Give a bounding box for every Plasmodium parasite, every leukocyte, and every artifact (stain precipitate or debris).
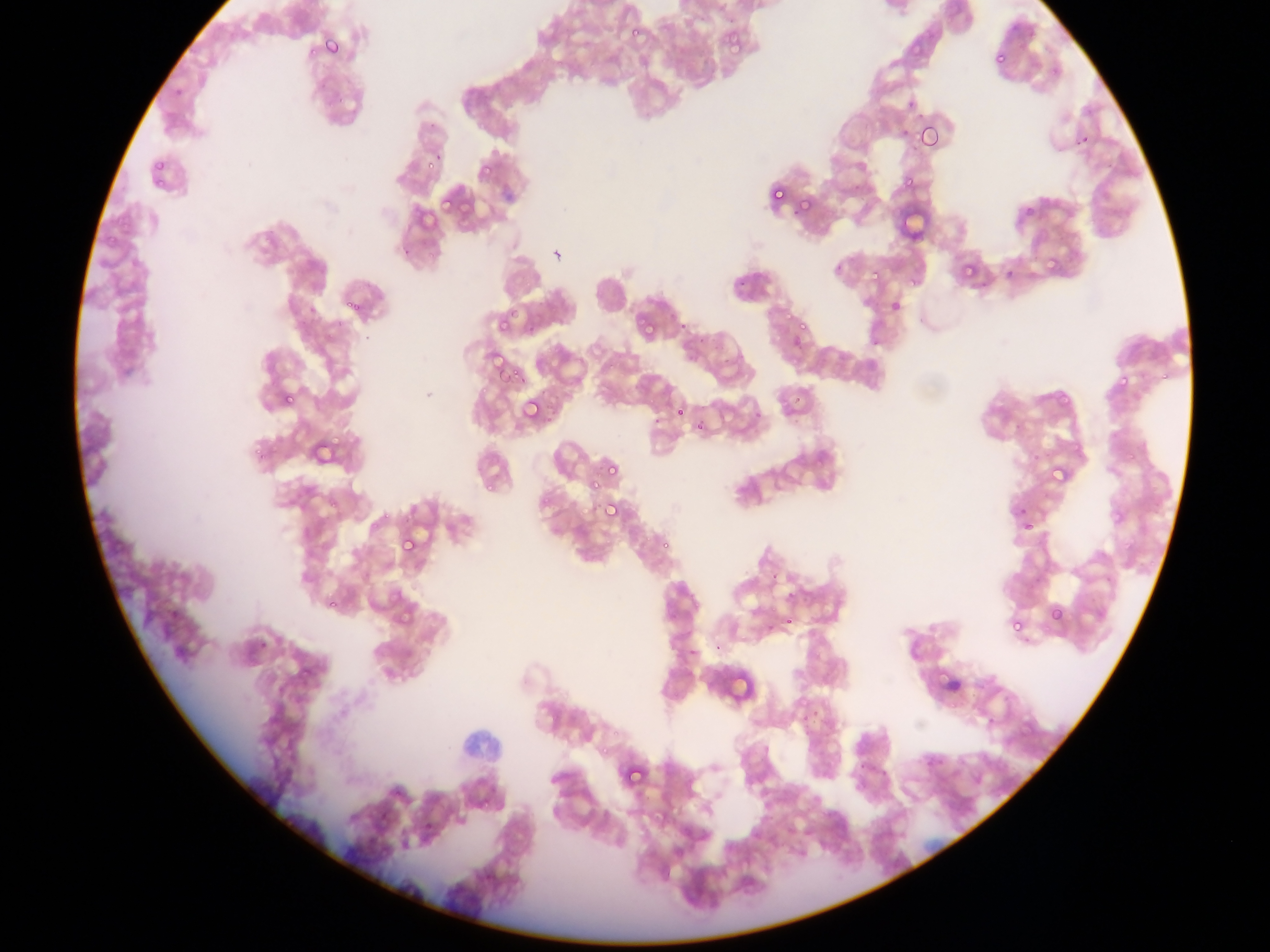

Approximate bounding boxes as [left, top, right, bottom] in pixels.
Plasmodium parasites: [626, 24, 648, 47], [719, 28, 744, 53], [312, 29, 347, 65], [904, 42, 925, 59], [990, 45, 1011, 67], [993, 51, 1007, 65], [917, 122, 943, 152], [150, 154, 172, 173], [899, 168, 917, 189], [770, 186, 786, 205], [803, 192, 816, 219], [435, 197, 461, 214], [1025, 207, 1036, 219], [411, 213, 442, 236], [958, 253, 983, 291], [1042, 256, 1059, 273], [870, 270, 887, 287], [344, 290, 375, 325], [887, 297, 905, 317], [781, 314, 793, 322], [640, 315, 664, 340], [497, 316, 518, 333], [797, 320, 814, 331], [789, 334, 806, 352], [497, 362, 526, 388], [1113, 370, 1145, 386], [1052, 382, 1077, 410], [278, 391, 295, 410], [520, 396, 544, 424], [674, 406, 688, 421], [694, 420, 709, 436], [604, 456, 617, 472], [1048, 461, 1073, 486], [601, 498, 623, 522], [1014, 503, 1033, 525], [1017, 517, 1035, 535], [396, 533, 418, 558], [399, 599, 422, 625], [166, 604, 182, 621], [1047, 604, 1067, 625], [783, 612, 799, 628], [1010, 616, 1023, 632], [622, 762, 646, 789].
No leukocytes observed.

Summary:
  - Capture: mobile-phone photograph through a microscope
  - Image size: 1270×952 pixels
  - Country: Ghana
  - Preparation: thin blood film
  - Field of view: single